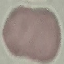
Summary:
  - Malaria status: uninfected
  - Stain: Giemsa
  - Image type: cell patch, automatically extracted from a larger field of view and resized to 64 × 64 pixels
  - Preparation: thin smear
  - Capture: smartphone through the microscope eyepiece